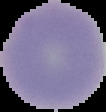
Summary:
  - Preparation: thin blood film
  - Image size: 106×112 pixels
  - Malaria status: uninfected
  - Image type: cell region segmented out of the field of view; surrounding area masked to black